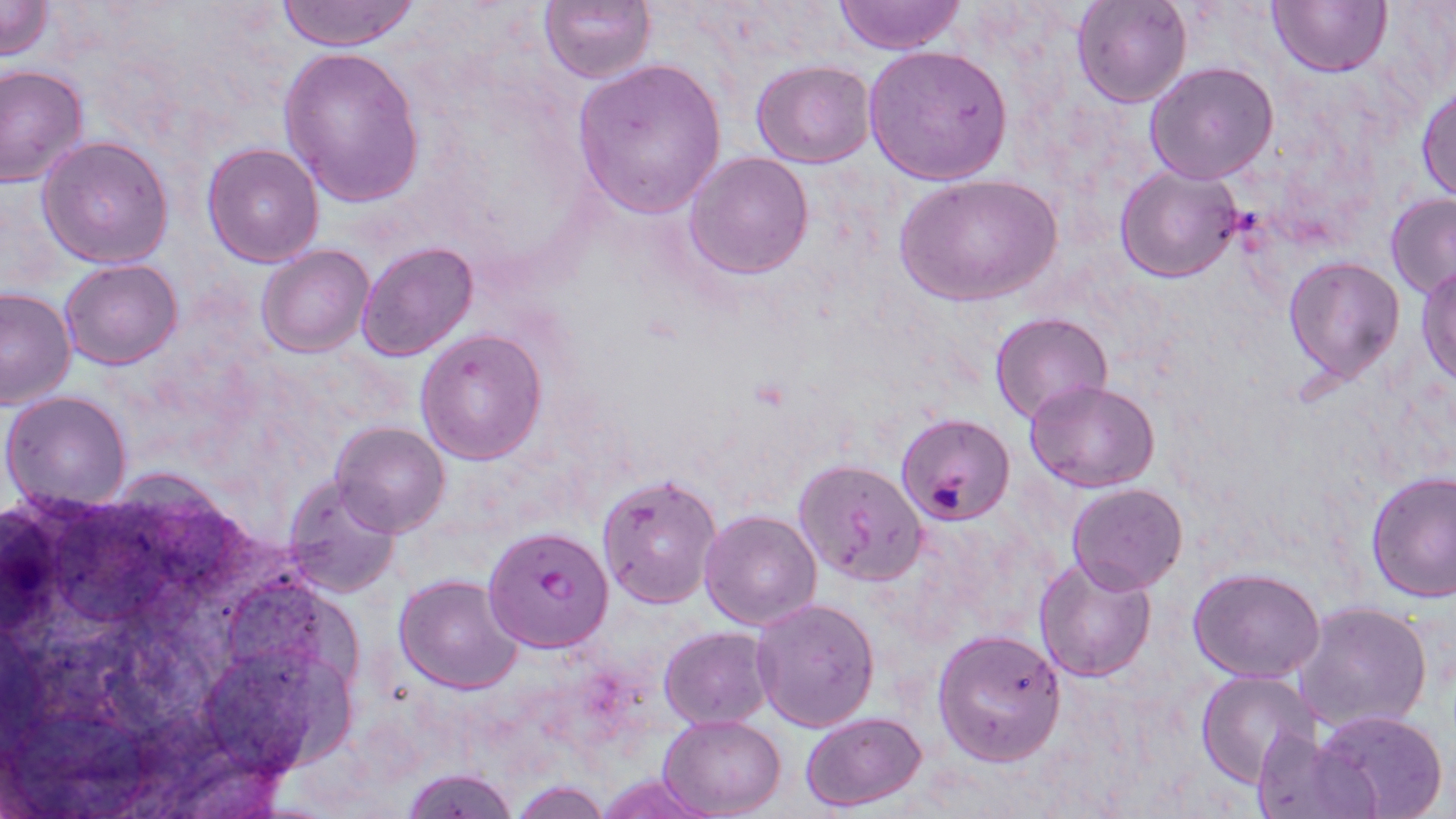
{
  "slide_level_diagnosis": "Plasmodium falciparum",
  "modality": "optical microscopy",
  "uninfected_red_blood_cell_locations": "approximate bounding boxes as named x1/y1/x2/y2 corners in pixels: (x1=0, y1=0, x2=54, y2=60), (x1=275, y1=0, x2=424, y2=51), (x1=537, y1=0, x2=657, y2=84), (x1=832, y1=0, x2=968, y2=53), (x1=1073, y1=0, x2=1192, y2=108), (x1=1267, y1=0, x2=1391, y2=76), (x1=862, y1=43, x2=1014, y2=186), (x1=278, y1=45, x2=425, y2=206), (x1=572, y1=58, x2=727, y2=219), (x1=751, y1=60, x2=875, y2=167), (x1=1145, y1=61, x2=1279, y2=185), (x1=0, y1=63, x2=90, y2=186), (x1=1418, y1=83, x2=1456, y2=203), (x1=37, y1=135, x2=172, y2=267), (x1=201, y1=143, x2=324, y2=265), (x1=684, y1=150, x2=815, y2=279), (x1=1114, y1=164, x2=1242, y2=283), (x1=895, y1=171, x2=1062, y2=307), (x1=1385, y1=193, x2=1456, y2=300), (x1=357, y1=241, x2=479, y2=361), (x1=257, y1=244, x2=375, y2=359), (x1=1282, y1=255, x2=1405, y2=385), (x1=59, y1=258, x2=183, y2=369), (x1=1417, y1=263, x2=1456, y2=388), (x1=0, y1=286, x2=78, y2=409), (x1=989, y1=312, x2=1112, y2=424), (x1=415, y1=328, x2=547, y2=465), (x1=1027, y1=380, x2=1159, y2=492), (x1=2, y1=390, x2=133, y2=510), (x1=897, y1=414, x2=1016, y2=525), (x1=332, y1=422, x2=450, y2=535), (x1=794, y1=459, x2=927, y2=585), (x1=1365, y1=470, x2=1455, y2=603), (x1=597, y1=471, x2=722, y2=609), (x1=280, y1=474, x2=404, y2=596), (x1=1067, y1=483, x2=1187, y2=594), (x1=698, y1=509, x2=821, y2=630), (x1=1034, y1=555, x2=1158, y2=682), (x1=1189, y1=568, x2=1327, y2=680), (x1=394, y1=573, x2=526, y2=694), (x1=750, y1=597, x2=881, y2=732), (x1=1294, y1=601, x2=1433, y2=734), (x1=659, y1=627, x2=772, y2=729), (x1=932, y1=628, x2=1067, y2=765), (x1=1196, y1=672, x2=1324, y2=787), (x1=1314, y1=709, x2=1451, y2=819), (x1=799, y1=712, x2=927, y2=810), (x1=658, y1=716, x2=785, y2=818), (x1=1250, y1=730, x2=1378, y2=819), (x1=399, y1=768, x2=520, y2=819), (x1=594, y1=771, x2=715, y2=819), (x1=507, y1=780, x2=614, y2=817)",
  "magnification": "1000x",
  "plasmodium_falciparum_infected_red_blood_cell_locations": "approximate bounding boxes as named x1/y1/x2/y2 corners in pixels: (x1=484, y1=523, x2=615, y2=653)",
  "image_size": "1456×819 pixels",
  "preparation": "thin blood film",
  "stain": "May-Grünwald-Giemsa",
  "field_of_view": "one of a larger specimen"
}